Identify the parasite.
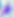
This is Toxoplasma gondii.

Summary:
  - Modality: micrograph
  - Magnification: 400x